State which cell type is depicted.
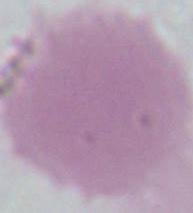

This is an erythrocyte.

1000x magnification. Photomicrograph.